Comment on the morphology of the red blood cells.
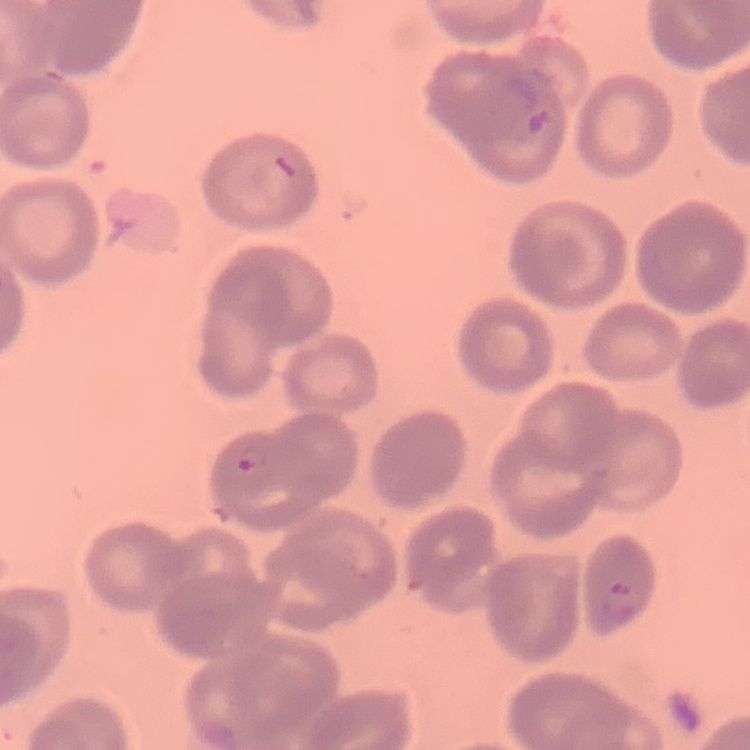

No rouleaux formation.

Summary:
  - Stain: Field's or Giemsa
  - Preparation: thin blood smear
  - Image type: one tile cut from a larger photomicrograph